Point out each Plasmodium parasite.
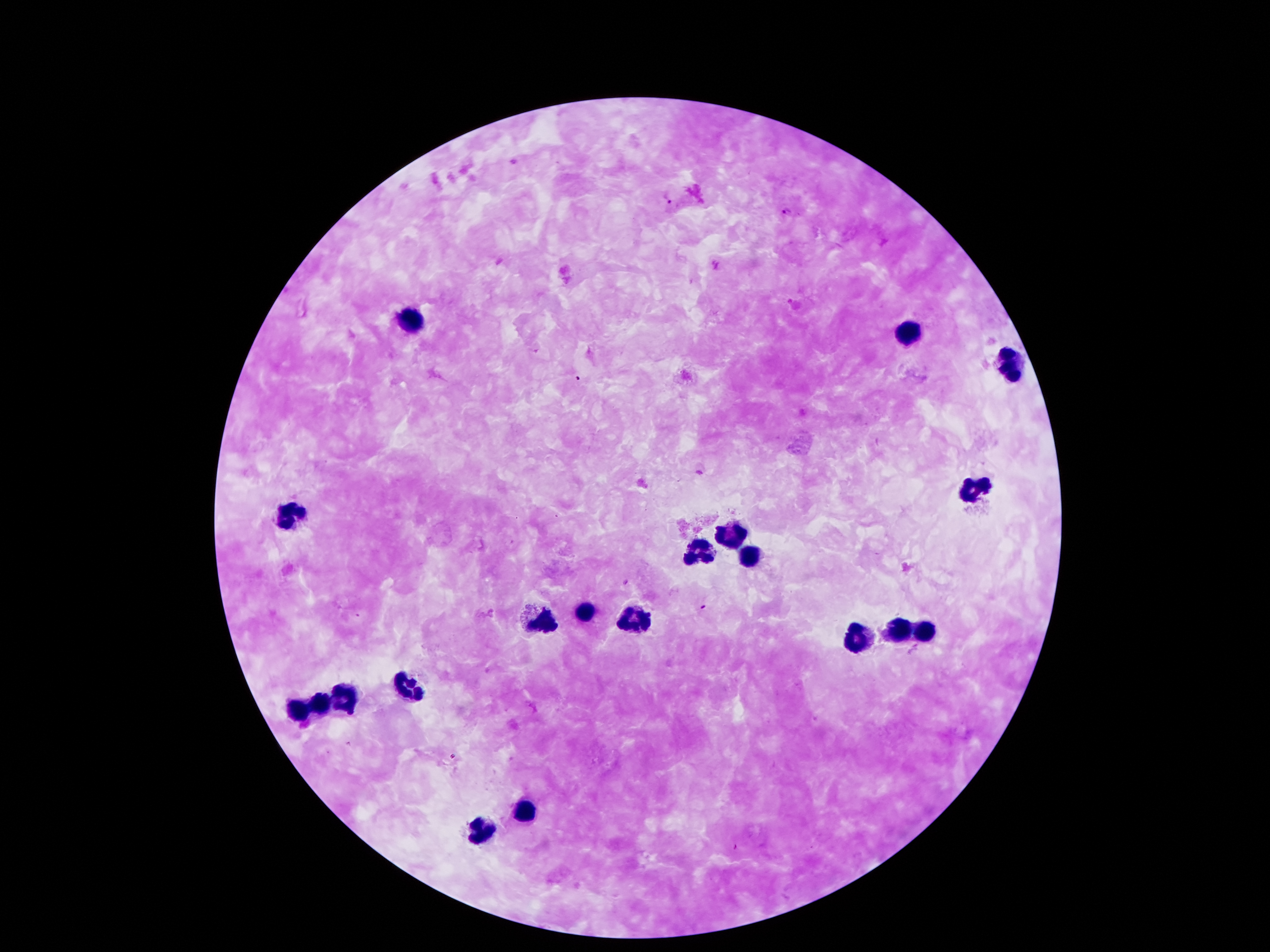
Approximate centers as [x, y] in pixels.
Plasmodium parasites: [667, 197], [786, 213], [792, 303], [627, 583], [702, 605], [453, 756].

Leukocyte locations: [413, 322], [909, 336], [1011, 363], [975, 489], [289, 519], [727, 537], [697, 557], [749, 559], [587, 611], [547, 621], [639, 623], [901, 630], [925, 633], [855, 641], [409, 689], [349, 697], [317, 703], [303, 712], [525, 814], [481, 834]. One field from this slide. Image is 1270×952 pixels. Giemsa-stained preparation. Thick blood film. Photographed through the microscope eyepiece with a smartphone camera. 100x magnification. Patient malaria status: positive for Plasmodium falciparum.